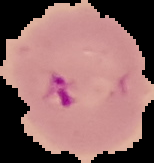

malaria status = parasitized
preparation = thin blood smear
image size = 154×163 pixels
image type = segmented cell region on a black background